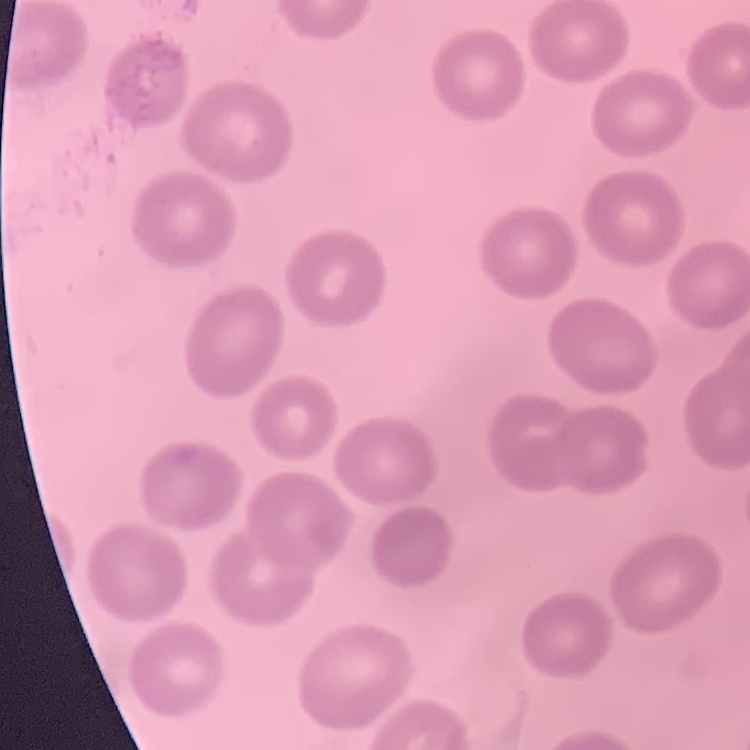
Summary:
  - Red blood cell morphology: no rouleaux formation
  - Stain: Field's or Giemsa
  - Preparation: thin peripheral smear
  - Image type: square crop of a larger photomicrograph